Report the malaria status of this cell.
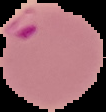
Parasitized.

Summary:
  - Image type: segmented cell region with the area outside set to black
  - Preparation: thin blood smear
  - Image size: 106×112 pixels